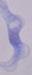
Photomicrograph. Captured at 1000x magnification. A trypanosome is seen.